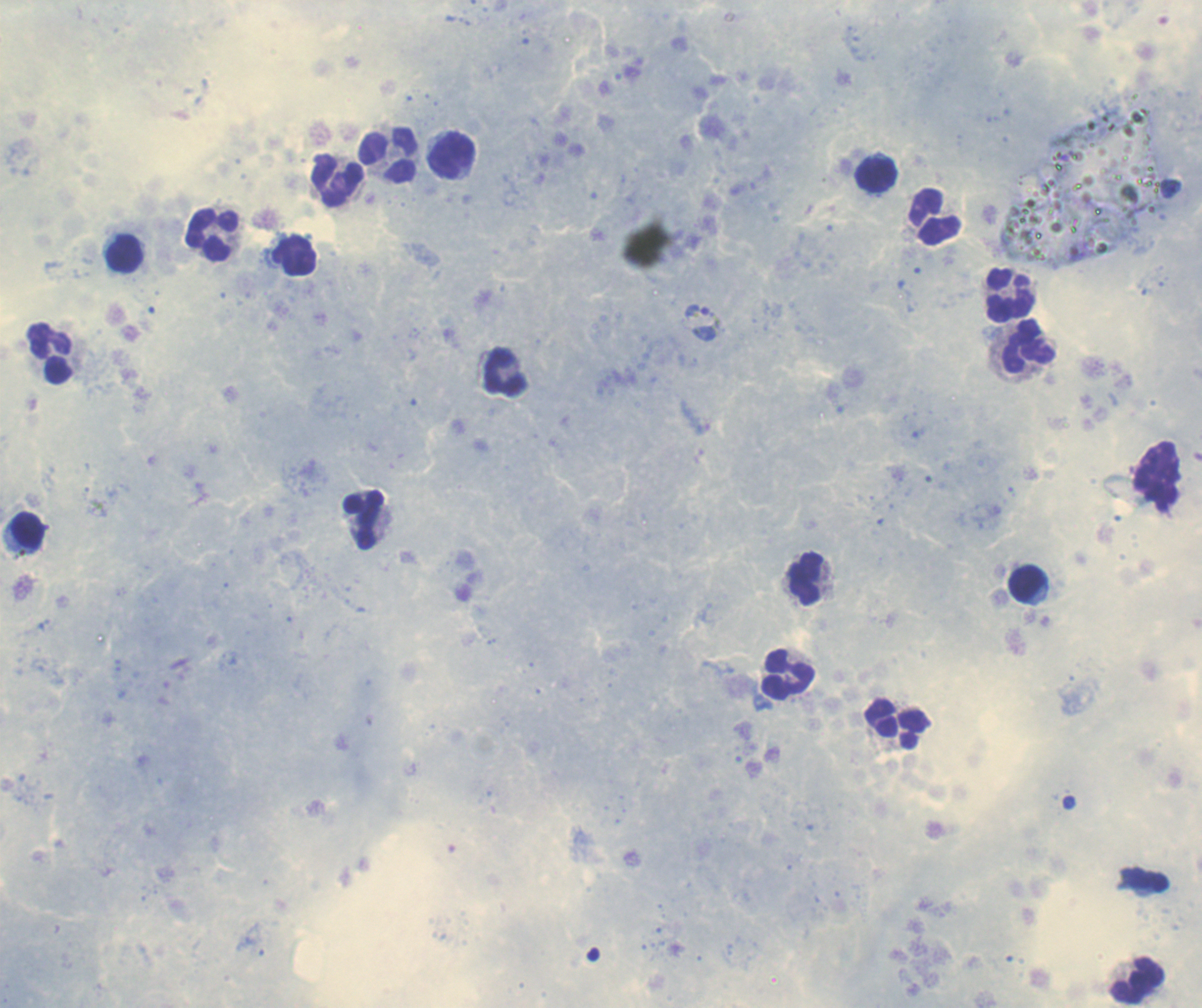
coordinate format = approximate centers as {x, y} in pixels
leukocyte locations = {389, 156}, {451, 156}, {876, 176}, {338, 180}, {935, 218}, {211, 236}, {125, 254}, {294, 256}, {1010, 295}, {1029, 346}, {49, 354}, {505, 374}, {363, 521}, {28, 531}, {805, 581}, {1027, 584}, {788, 676}, {897, 725}, {1139, 981}
trophozoite locations = {704, 322}
context = previously used in an actual diagnosis
coloration quality = good
result = positive for Plasmodium parasites
stain = Romanowsky
image size = 1202×1008 pixels
preparation = thick blood smear
background quality = satisfactory
field of view = single
magnification = 100x